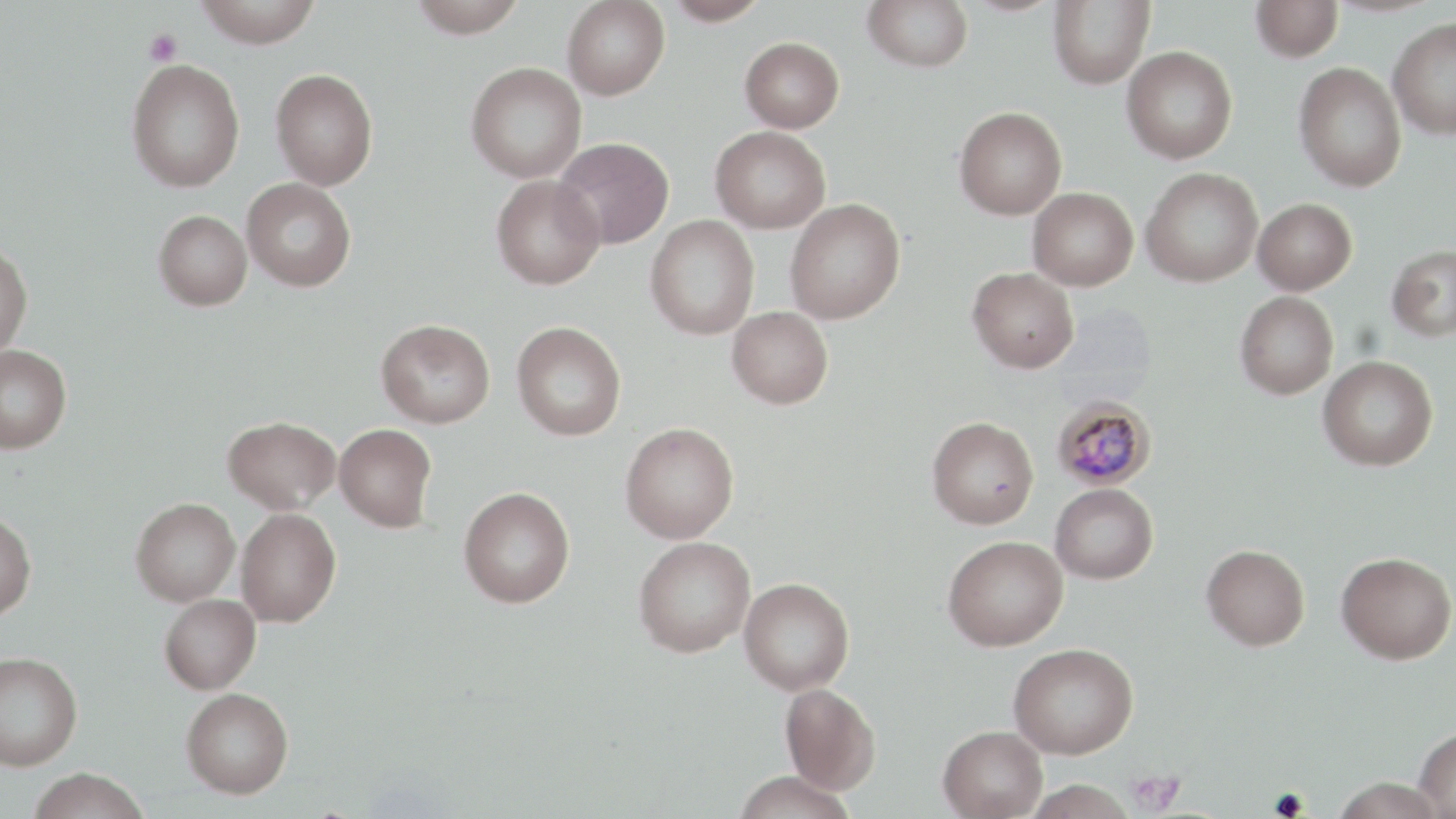

slide_level_diagnosis: Plasmodium malariae
image_size: 1456×819 pixels
preparation: thin blood film
stain: May-Grünwald-Giemsa
plasmodium_malariae_infected_red_blood_cell_locations: 'approximate bounding boxes as (x1, y1, x2, y2) in pixels: (1052, 395, 1157, 490)'
magnification: 1000x
field_of_view: single
modality: optical microscopy
uninfected_red_blood_cell_locations: 'approximate bounding boxes as (x1, y1, x2, y2) in pixels: (192, 0, 324, 48), (408, 0, 528, 37), (663, 0, 771, 26), (863, 0, 974, 72), (1048, 0, 1155, 89), (1251, 0, 1343, 62), (562, 1, 670, 100), (1387, 18, 1456, 139), (739, 37, 844, 132), (1122, 45, 1238, 164), (126, 59, 246, 191), (465, 61, 587, 183), (1294, 62, 1407, 191), (270, 68, 378, 189), (954, 106, 1067, 220), (710, 125, 831, 233), (552, 136, 674, 249), (1140, 167, 1263, 287), (491, 175, 605, 290), (241, 178, 356, 291), (1027, 187, 1138, 290), (1253, 198, 1357, 295), (785, 199, 905, 325), (153, 209, 252, 311), (645, 215, 760, 341), (0, 240, 33, 357), (1386, 244, 1456, 342), (967, 267, 1079, 373), (1235, 291, 1339, 399), (727, 306, 833, 408), (376, 319, 495, 428), (512, 321, 626, 440), (0, 344, 72, 454), (1318, 355, 1438, 471), (223, 415, 340, 513), (927, 416, 1039, 528), (620, 422, 739, 542), (335, 423, 437, 531), (1050, 483, 1158, 584), (459, 487, 575, 607), (131, 498, 240, 606), (236, 507, 341, 626), (0, 510, 36, 620), (943, 535, 1069, 650), (633, 536, 756, 657), (1202, 544, 1310, 650), (1336, 551, 1455, 664), (739, 577, 854, 695), (160, 593, 261, 694), (1008, 643, 1138, 759), (0, 650, 83, 770), (780, 683, 880, 794), (181, 687, 294, 798), (938, 725, 1047, 819), (1414, 726, 1456, 818), (27, 768, 149, 819), (732, 770, 857, 819), (1331, 777, 1446, 819), (1024, 779, 1137, 819)'
platelet_locations: 'approximate bounding boxes as (x1, y1, x2, y2) in pixels: (143, 29, 183, 66), (1125, 770, 1185, 814)'